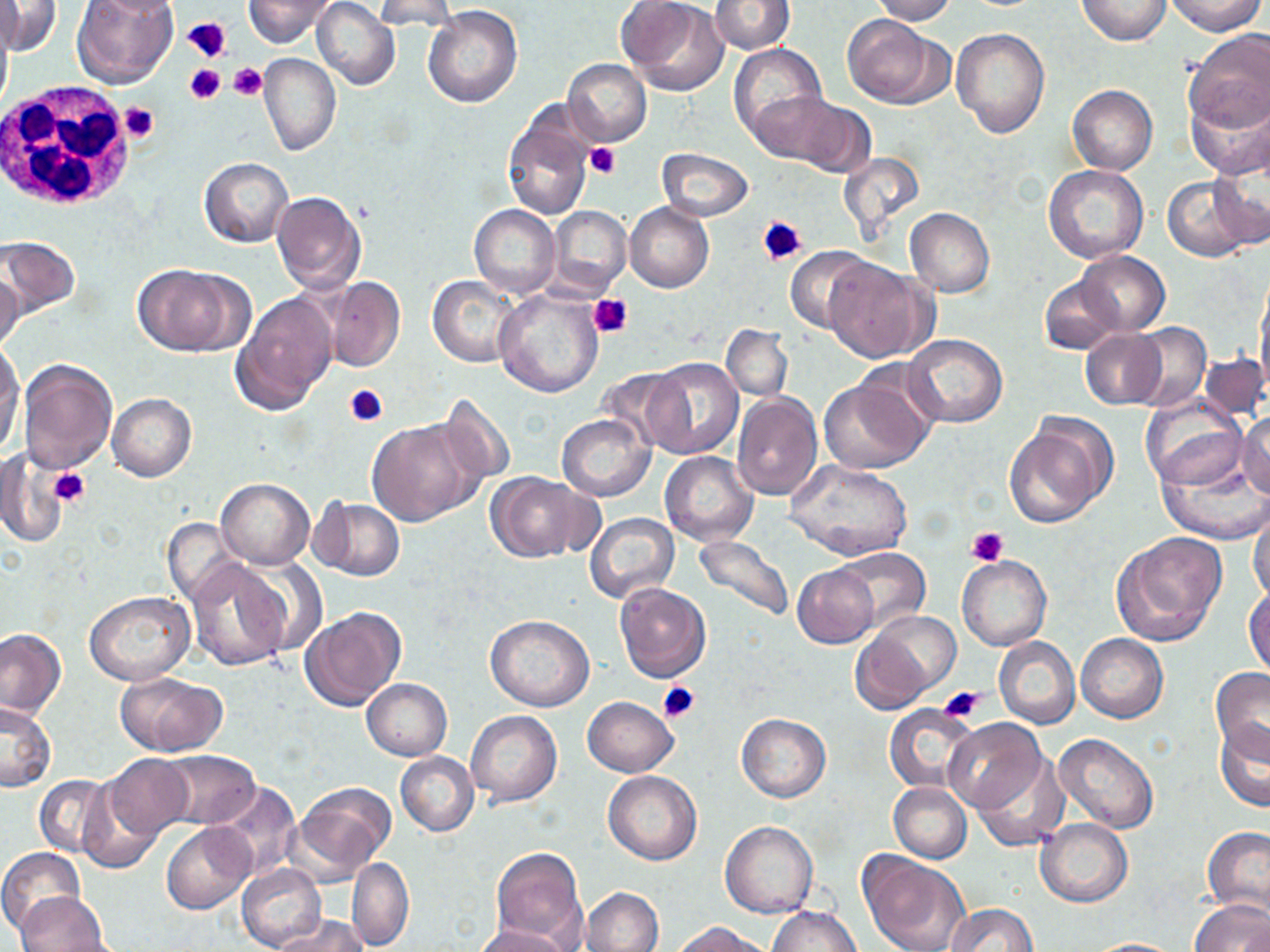

Summary:
  - Coordinate format: approximate bounding boxes as (x1, y1, x2, y2) in pixels
  - Platelet locations: (184, 16, 231, 65), (230, 62, 267, 101), (184, 65, 224, 102), (118, 102, 158, 143), (586, 142, 621, 179), (758, 215, 808, 267), (589, 292, 632, 338), (345, 384, 390, 429), (48, 467, 90, 507), (967, 527, 1008, 566), (658, 681, 700, 723), (938, 685, 984, 721)
  - Uninfected red blood cell locations: (71, 0, 177, 89), (243, 0, 337, 49), (312, 0, 399, 90), (371, 0, 460, 31), (622, 0, 729, 96), (707, 0, 794, 53), (868, 0, 958, 23), (1075, 0, 1173, 46), (1165, 0, 1266, 36), (1, 2, 60, 58), (423, 6, 522, 108), (0, 13, 13, 113), (844, 14, 946, 108), (950, 27, 1050, 140), (1183, 29, 1270, 134), (729, 43, 827, 143), (257, 53, 340, 156), (562, 58, 651, 146), (1067, 84, 1157, 175), (1185, 89, 1270, 179), (750, 90, 848, 167), (783, 97, 878, 179), (501, 108, 595, 220), (657, 148, 752, 221), (1210, 149, 1270, 248), (836, 150, 927, 242), (199, 157, 293, 247), (1043, 165, 1150, 264), (1162, 176, 1256, 261), (271, 191, 367, 294), (625, 203, 715, 292), (469, 204, 560, 298), (548, 206, 631, 296), (905, 207, 995, 297), (0, 235, 80, 317), (786, 247, 870, 331), (1075, 251, 1169, 335), (823, 258, 934, 361), (131, 264, 251, 357), (0, 267, 26, 352), (429, 275, 523, 368), (1039, 275, 1121, 355), (322, 276, 405, 373), (1255, 280, 1269, 399), (493, 287, 604, 397), (232, 292, 338, 414), (1127, 323, 1210, 412), (721, 325, 792, 400), (1081, 328, 1166, 410), (904, 333, 1008, 427), (0, 343, 23, 455), (1199, 354, 1269, 422), (645, 357, 743, 459), (19, 358, 117, 476), (597, 366, 689, 450), (822, 369, 937, 474), (733, 392, 823, 501), (1139, 393, 1249, 489), (107, 394, 197, 481), (437, 394, 516, 488), (1238, 412, 1270, 499), (557, 413, 654, 500), (1004, 414, 1115, 529), (366, 418, 483, 526), (1155, 441, 1270, 544), (2, 448, 27, 546), (661, 451, 758, 545), (3, 455, 62, 547), (784, 459, 915, 563), (485, 471, 591, 563), (215, 478, 314, 569), (311, 497, 405, 581), (1249, 501, 1270, 605), (585, 512, 678, 603), (164, 517, 247, 607), (1111, 532, 1229, 646), (691, 534, 794, 626), (833, 547, 931, 633), (956, 554, 1052, 652), (186, 557, 294, 672), (792, 565, 879, 648), (615, 583, 711, 682), (1245, 586, 1270, 678), (84, 591, 194, 686), (301, 607, 407, 711), (866, 611, 962, 696), (485, 615, 595, 710), (0, 628, 66, 720), (850, 629, 933, 715), (1075, 633, 1168, 722), (994, 636, 1080, 729), (1210, 667, 1270, 758), (116, 672, 226, 755), (361, 678, 452, 760), (583, 696, 678, 776), (1, 702, 56, 793), (885, 705, 977, 795), (466, 710, 562, 807), (736, 713, 831, 802), (944, 718, 1044, 814), (1214, 719, 1270, 811), (1054, 733, 1158, 834), (157, 751, 262, 830), (395, 752, 478, 836), (971, 752, 1070, 852), (101, 754, 193, 839), (603, 771, 702, 865), (36, 775, 116, 857), (209, 781, 301, 881), (889, 782, 971, 863), (293, 783, 396, 880), (77, 786, 162, 873), (1035, 818, 1133, 908), (719, 820, 818, 918), (162, 822, 256, 915), (1203, 827, 1270, 919), (0, 846, 84, 935), (491, 847, 587, 950), (857, 852, 969, 952), (346, 857, 414, 950), (237, 864, 327, 952), (581, 886, 663, 952), (16, 891, 110, 952), (1190, 898, 1270, 952), (944, 903, 1037, 952), (769, 906, 861, 952), (275, 914, 367, 952), (676, 921, 769, 952), (471, 924, 574, 952), (1083, 938, 1187, 951)
  - White blood cell locations: (0, 81, 135, 213)
  - Slide-level diagnosis: negative for blood parasites
  - Image size: 1270×952 pixels
  - Preparation: thin blood smear
  - Stain: May-Grünwald-Giemsa
  - Magnification: 1000x
  - Modality: light microscopy
  - Field of view: single